State the blood parasite species.
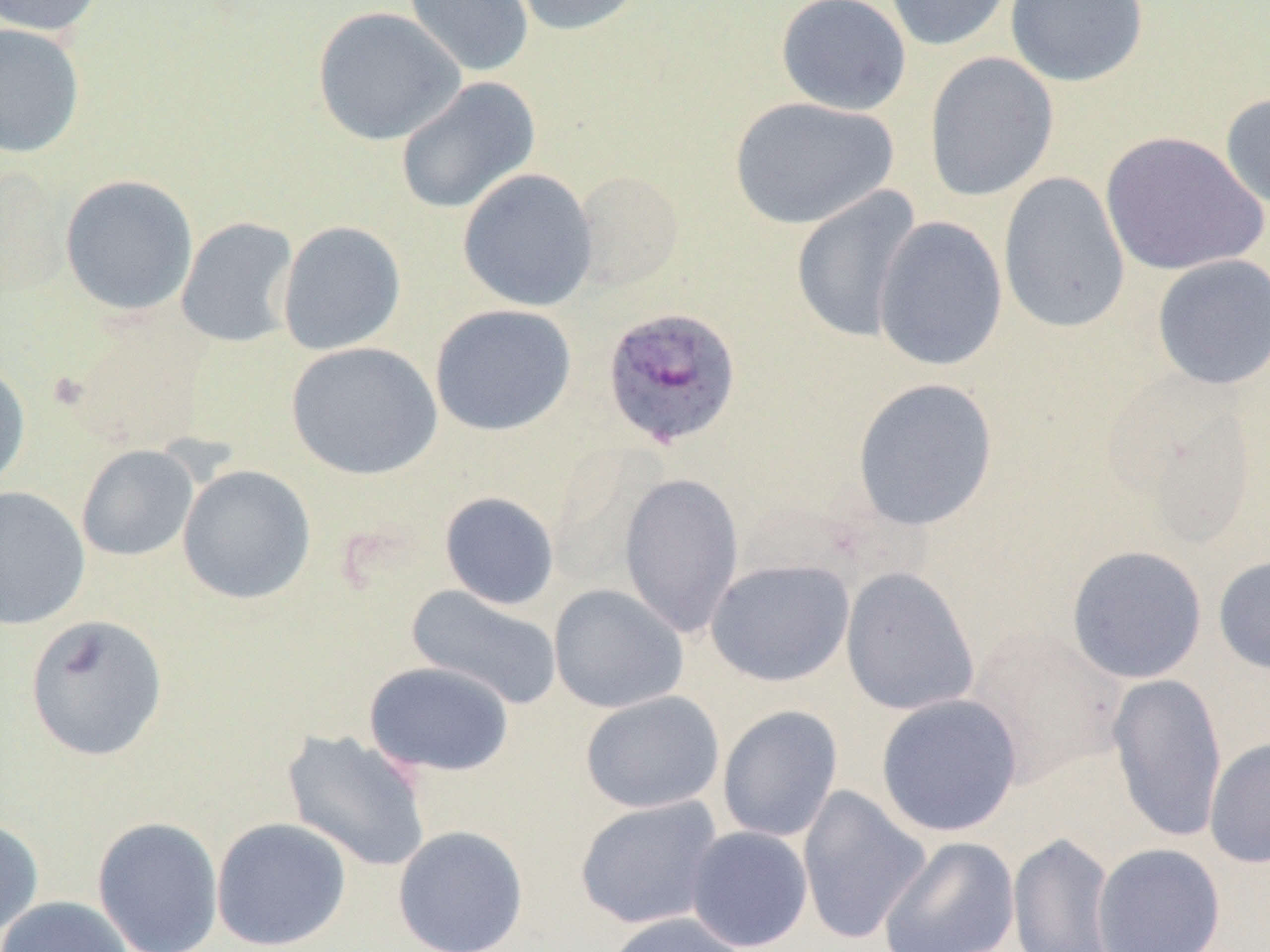
Plasmodium ovale.

Summary:
  - Coordinate format: approximate bounding boxes as named x1/y1/x2/y2 corners in pixels
  - Plasmodium ovale-infected red blood cell locations: (x1=600, y1=302, x2=743, y2=448)
  - Uninfected red blood cell locations: (x1=0, y1=0, x2=106, y2=37), (x1=402, y1=0, x2=534, y2=78), (x1=504, y1=0, x2=650, y2=36), (x1=776, y1=0, x2=912, y2=116), (x1=882, y1=0, x2=1015, y2=52), (x1=1006, y1=0, x2=1148, y2=88), (x1=312, y1=6, x2=465, y2=146), (x1=0, y1=22, x2=85, y2=158), (x1=924, y1=52, x2=1059, y2=202), (x1=395, y1=76, x2=541, y2=215), (x1=1219, y1=91, x2=1270, y2=212), (x1=728, y1=96, x2=899, y2=230), (x1=1099, y1=130, x2=1267, y2=276), (x1=457, y1=167, x2=598, y2=312), (x1=572, y1=169, x2=685, y2=293), (x1=998, y1=171, x2=1131, y2=334), (x1=60, y1=174, x2=198, y2=316), (x1=791, y1=186, x2=923, y2=344), (x1=873, y1=215, x2=1008, y2=372), (x1=176, y1=217, x2=300, y2=348), (x1=277, y1=220, x2=406, y2=356), (x1=1151, y1=254, x2=1270, y2=390), (x1=429, y1=303, x2=576, y2=437), (x1=66, y1=314, x2=211, y2=453), (x1=285, y1=341, x2=442, y2=480), (x1=0, y1=357, x2=31, y2=492), (x1=851, y1=377, x2=999, y2=531), (x1=76, y1=445, x2=199, y2=561), (x1=177, y1=464, x2=316, y2=605), (x1=619, y1=471, x2=744, y2=639), (x1=0, y1=486, x2=90, y2=629), (x1=439, y1=491, x2=560, y2=610), (x1=1066, y1=545, x2=1208, y2=684), (x1=1212, y1=554, x2=1270, y2=675), (x1=706, y1=558, x2=855, y2=686), (x1=841, y1=566, x2=980, y2=717), (x1=548, y1=583, x2=688, y2=714), (x1=405, y1=584, x2=562, y2=710), (x1=24, y1=613, x2=169, y2=762), (x1=964, y1=624, x2=1126, y2=786), (x1=364, y1=660, x2=515, y2=777), (x1=1107, y1=672, x2=1227, y2=843), (x1=580, y1=690, x2=725, y2=813), (x1=875, y1=693, x2=1023, y2=837), (x1=716, y1=705, x2=844, y2=843), (x1=281, y1=729, x2=432, y2=873), (x1=1204, y1=736, x2=1270, y2=869), (x1=796, y1=784, x2=931, y2=946), (x1=574, y1=794, x2=724, y2=930), (x1=0, y1=816, x2=44, y2=942), (x1=92, y1=816, x2=224, y2=952), (x1=211, y1=817, x2=352, y2=951), (x1=392, y1=825, x2=530, y2=952), (x1=685, y1=826, x2=814, y2=952), (x1=1007, y1=831, x2=1117, y2=952), (x1=878, y1=836, x2=1020, y2=952), (x1=1092, y1=842, x2=1227, y2=952), (x1=0, y1=896, x2=134, y2=952), (x1=601, y1=911, x2=750, y2=952)
  - Field of view: single
  - Image size: 1270×952 pixels
  - Preparation: thin blood film
  - Magnification: 1000x
  - Modality: light microscopy